Name the blood parasite species.
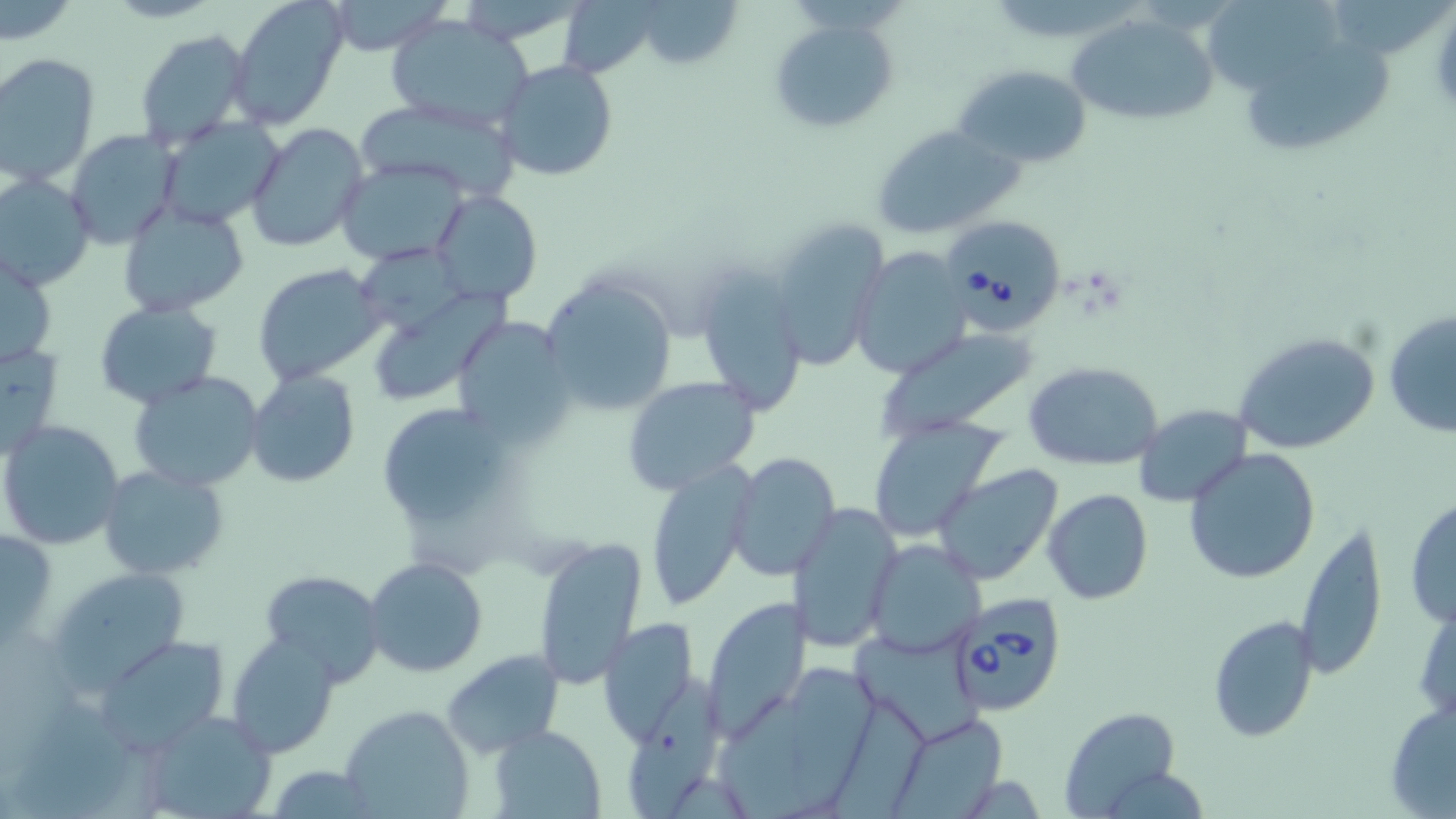
Babesia divergens.

Approximate bounding boxes as (x1, y1, x2, y2) in pixels. Babesia divergens-infected red blood cell locations: (945, 217, 1064, 333), (946, 593, 1070, 717). Uninfected red blood cell locations: (227, 0, 349, 130), (320, 0, 453, 56), (639, 1, 743, 66), (1208, 2, 1357, 100), (1068, 12, 1221, 126), (385, 14, 537, 131), (768, 16, 899, 135), (134, 28, 254, 151), (1251, 34, 1393, 154), (1, 52, 99, 186), (493, 58, 620, 183), (955, 65, 1095, 169), (353, 95, 524, 201), (157, 116, 285, 229), (245, 121, 370, 253), (871, 124, 1023, 240), (65, 128, 182, 248), (337, 158, 472, 266), (0, 173, 96, 293), (429, 187, 544, 306), (116, 201, 250, 317), (768, 217, 890, 368), (352, 243, 472, 332), (1, 244, 59, 373), (849, 247, 971, 378), (692, 261, 808, 419), (251, 263, 386, 386), (541, 275, 678, 418), (374, 290, 515, 398), (94, 301, 224, 407), (1382, 308, 1456, 440), (450, 314, 576, 445), (876, 328, 1038, 439), (1230, 331, 1381, 456), (0, 339, 66, 460), (1024, 360, 1165, 470), (244, 370, 361, 489), (130, 371, 265, 492), (622, 377, 762, 498), (378, 403, 512, 524), (1134, 404, 1253, 507), (866, 414, 1007, 541), (2, 420, 125, 551), (1184, 449, 1320, 584), (727, 451, 841, 579), (645, 461, 756, 609), (932, 464, 1064, 585), (97, 465, 230, 581), (1044, 489, 1153, 604), (1404, 498, 1455, 629), (788, 503, 903, 654), (1295, 519, 1388, 680), (2, 525, 55, 656), (534, 537, 648, 687), (866, 540, 985, 658), (363, 557, 488, 677), (44, 565, 194, 697), (260, 571, 385, 686), (700, 597, 812, 742), (1413, 597, 1456, 726), (1207, 614, 1318, 743), (595, 617, 701, 744), (851, 623, 977, 743), (227, 632, 339, 758), (99, 635, 230, 752), (442, 650, 563, 758), (789, 656, 884, 815), (625, 677, 723, 816), (720, 693, 827, 819), (1384, 699, 1456, 818), (341, 703, 476, 819), (1060, 706, 1183, 816), (135, 708, 279, 819), (889, 712, 1007, 818), (490, 723, 607, 817), (262, 765, 379, 818). May-Grünwald-Giemsa-stained preparation. Optical microscopy. One field of a larger specimen. 1000x magnification. Image is 1456×819 pixels. Thin blood smear.